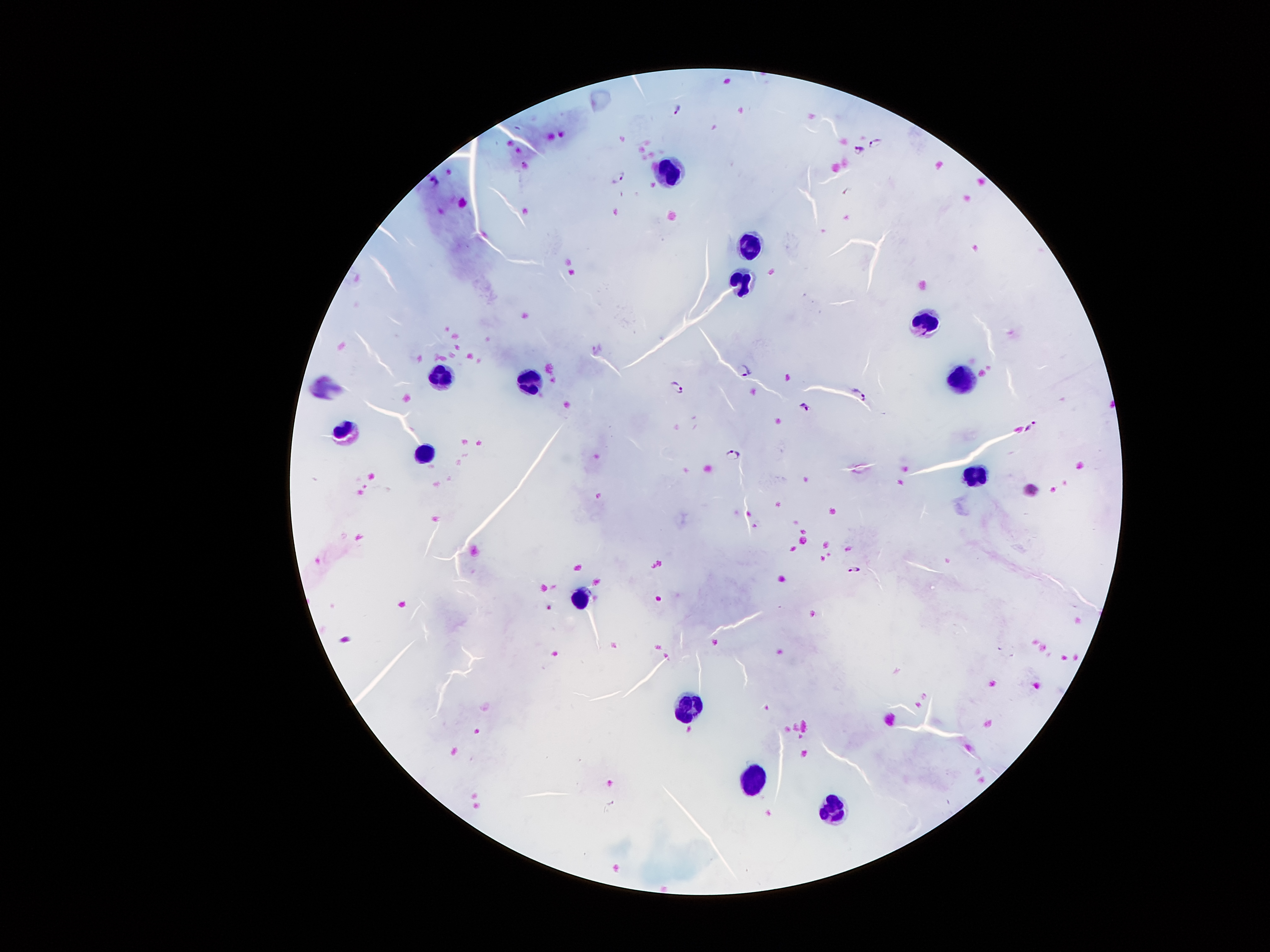
{
  "stain": "Giemsa",
  "preparation": "thick blood smear",
  "image_size": "1270×952 pixels",
  "capture": "smartphone through the microscope eyepiece",
  "malaria_parasite_locations": "approximate centers as {x, y} in pixels: {678, 109}, {875, 142}, {859, 149}, {619, 177}, {598, 350}, {747, 369}, {677, 388}, {859, 394}, {803, 406}, {1032, 427}, {734, 455}, {853, 570}",
  "field_of_view": "one from this slide",
  "magnification": "100x",
  "patient_malaria_status": "infected with Plasmodium falciparum",
  "leukocyte_locations": "approximate centers as {x, y} in pixels: {668, 172}, {749, 244}, {741, 280}, {935, 323}, {441, 376}, {530, 381}, {962, 383}, {341, 432}, {425, 451}, {976, 474}, {578, 601}, {690, 709}, {751, 788}, {833, 811}"
}